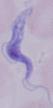

Summary:
  - Magnification: 1000x
  - Identification: trypanosome
  - Modality: micrograph